Classify this cell by malaria status.
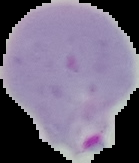
Parasitized.

image size = 139×163 pixels
preparation = thin blood film
image type = segmented cell region with the area outside set to black